Give the preparation type.
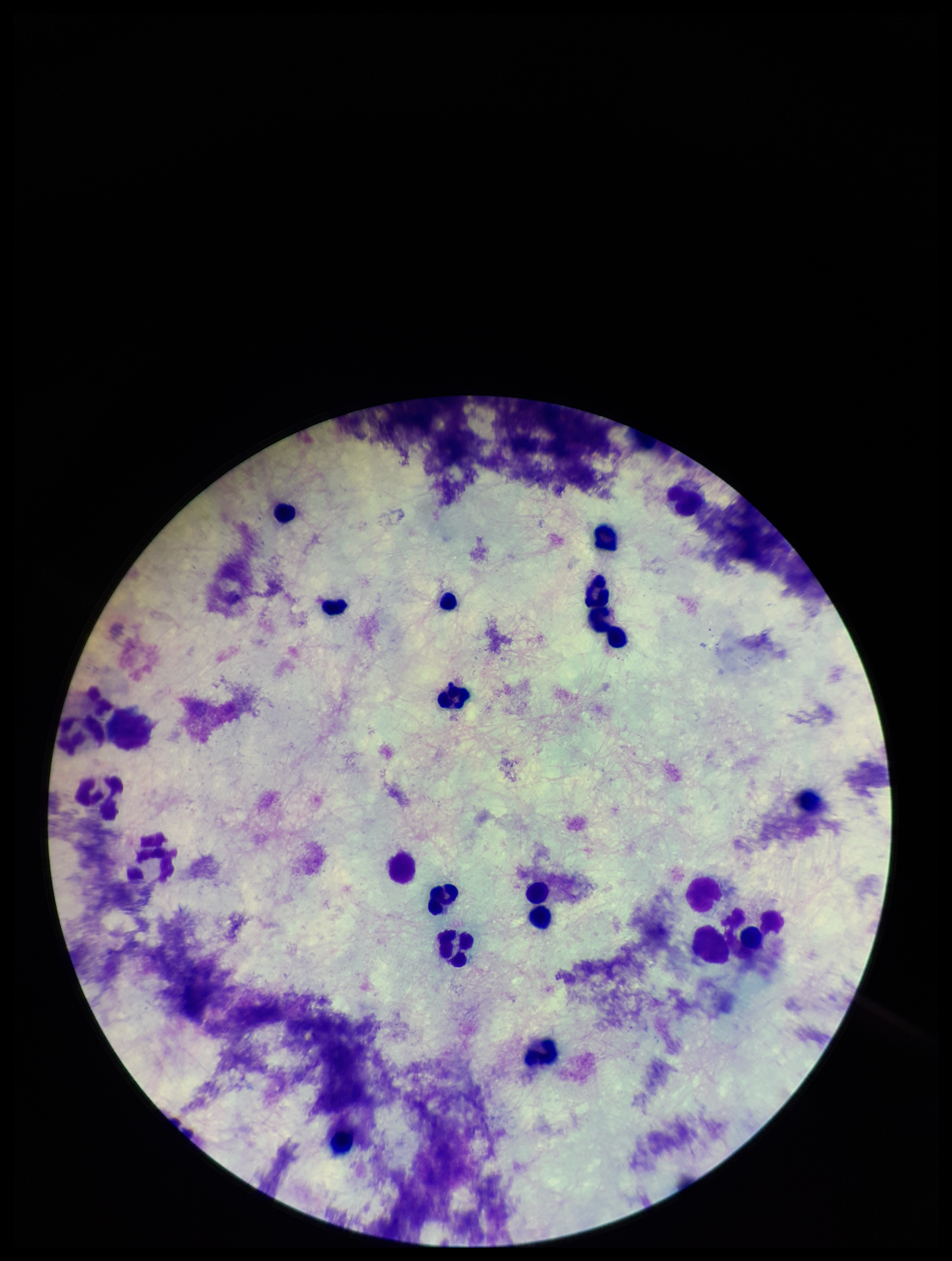

Thick.

Summary:
  - Image size: 952×1261 pixels
  - Stain: Giemsa
  - Plasmodium parasites: none seen
  - Capture: smartphone photograph through the microscope eyepiece
  - Leukocyte count: 21
  - Parasite count: 0
  - Field of view: one from this slide
  - Patient malaria status: negative